Report the malaria status of this cell.
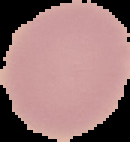

Uninfected.

image_type: cell region segmented out of the field of view; surrounding area masked to black
image_size: 130×142 pixels
preparation: thin blood film